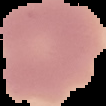
image size = 106×106 pixels
image type = cell region segmented out of the field of view; surrounding area masked to black
preparation = thin blood smear
result = no Plasmodium parasites seen